Assess this cell for malaria.
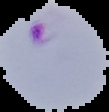

It is parasitized.

image type = segmented cell region on a black background
image size = 109×112 pixels
preparation = thin blood smear